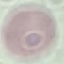

malaria status = uninfected
preparation = thin smear
capture = smartphone camera at the microscope eyepiece
image type = cell patch, automatically extracted from a larger field of view and resized to 64 × 64 pixels
stain = Giemsa